Name the cell type shown.
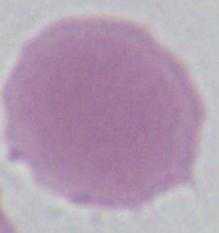
An erythrocyte.

Photomicrograph. Captured at 1000x magnification.